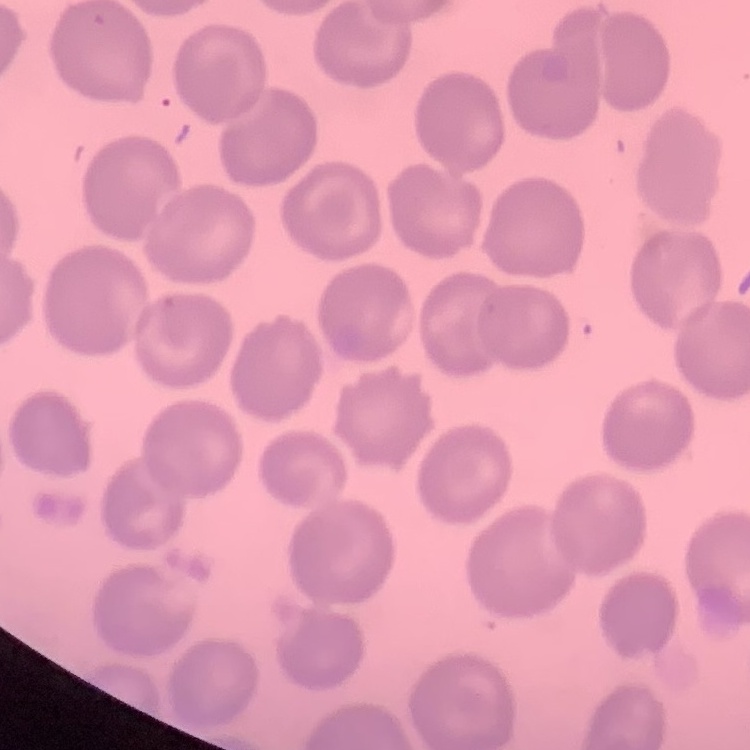

erythrocyte morphology = no rouleaux formation
image type = one tile cut from a larger photomicrograph
preparation = thin blood film
stain = Field's or Giemsa